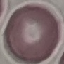

Result: no malaria parasites detected. Thin blood smear. Automatically extracted cell patch, resized to 64 × 64 pixels. Acquired by smartphone through the microscope eyepiece. Giemsa-stained preparation.